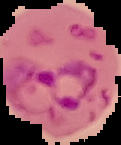

malaria status = parasitized
image size = 121×145 pixels
preparation = thin blood smear
image type = segmented cell region on a black background